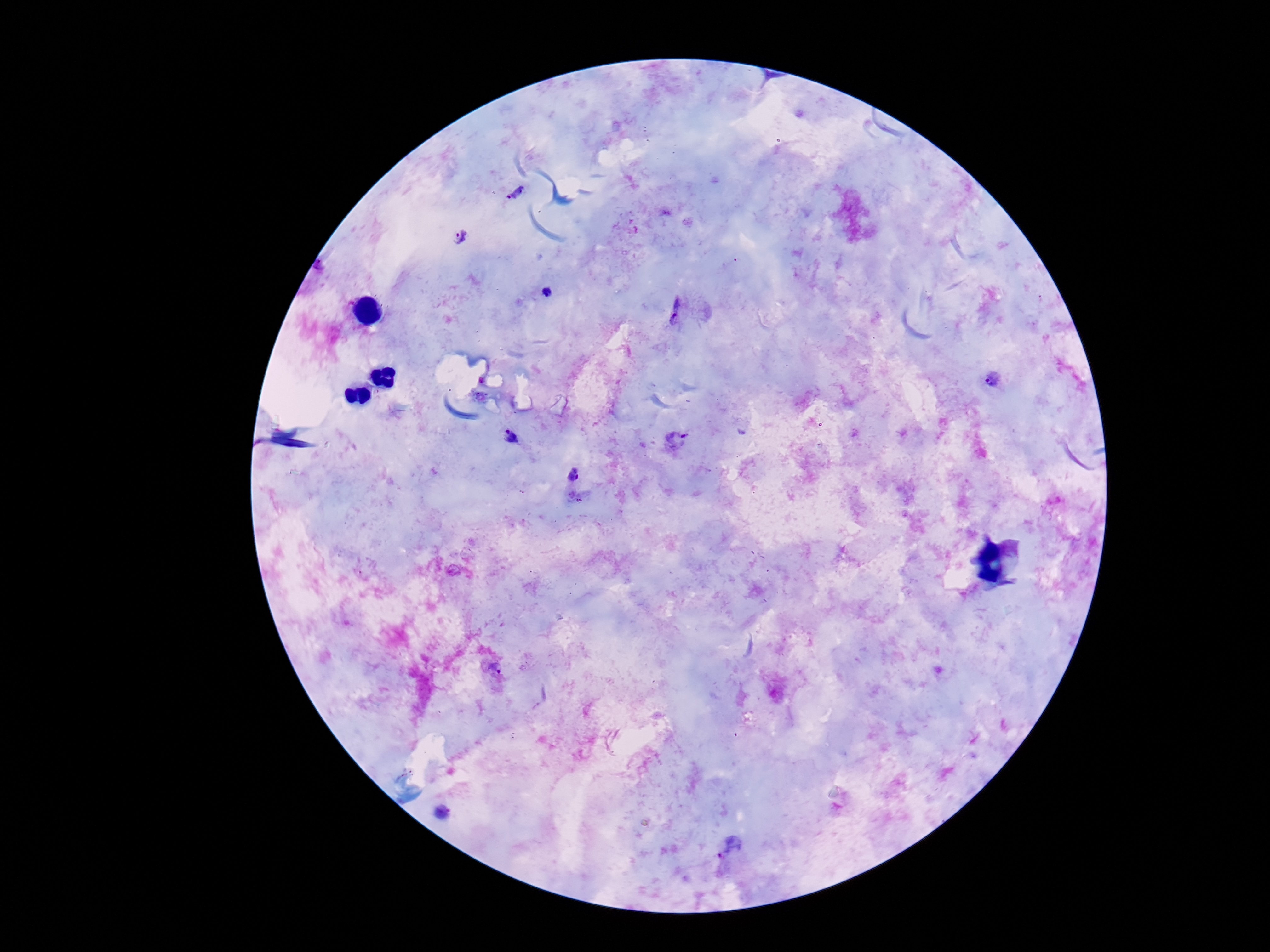

Approximate centers as [x, y] in pixels.
Summary:
  - Plasmodium parasite locations: [515, 192], [460, 237], [546, 293], [675, 310], [993, 379], [509, 437], [676, 441], [495, 667], [731, 847]
  - Preparation: thick peripheral-blood smear
  - Image size: 1270×952 pixels
  - Magnification: 100x
  - Capture: smartphone camera through the microscope eyepiece
  - Patient malaria status: positive
  - Stain: Giemsa
  - Field of view: one from this slide